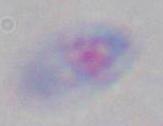 Captured at 1000x magnification. Photomicrograph. Toxoplasma gondii is seen.